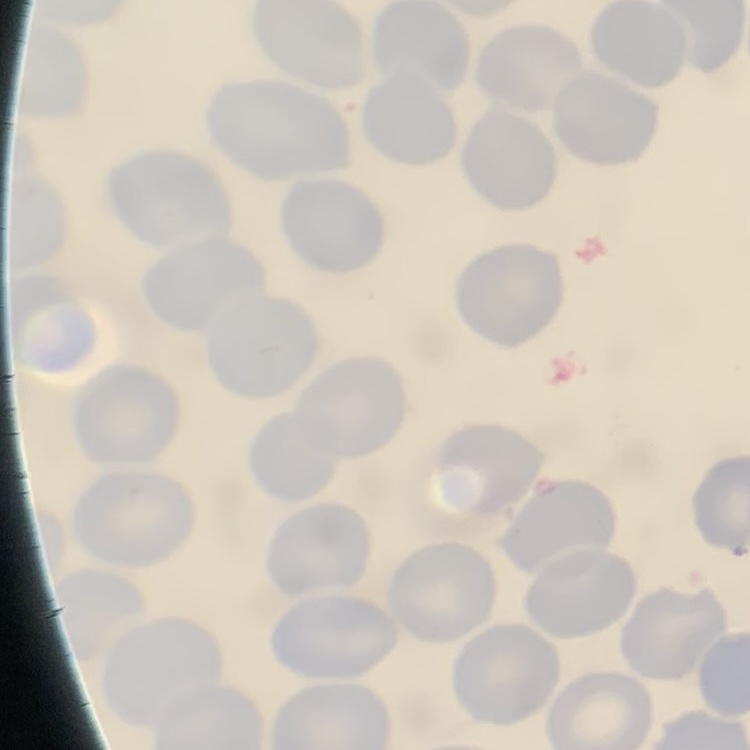 The red blood cells exhibit no rouleaux formation. Thin blood film. One tile cut from a larger photomicrograph. Stained with either Field's or Giemsa.